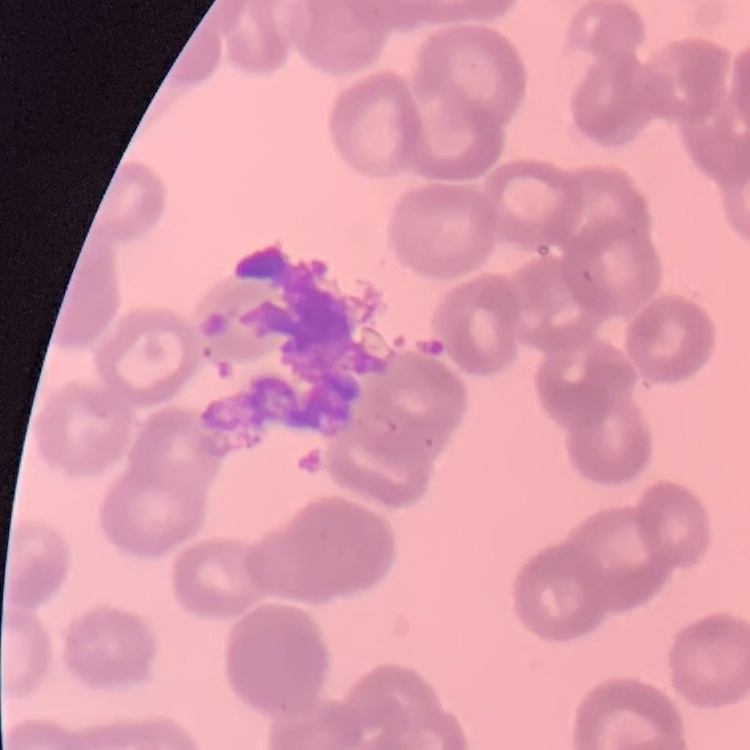

The erythrocytes exhibit rouleaux formation. Thin peripheral smear. One tile cut from a larger photomicrograph. Field's or Giemsa stain.